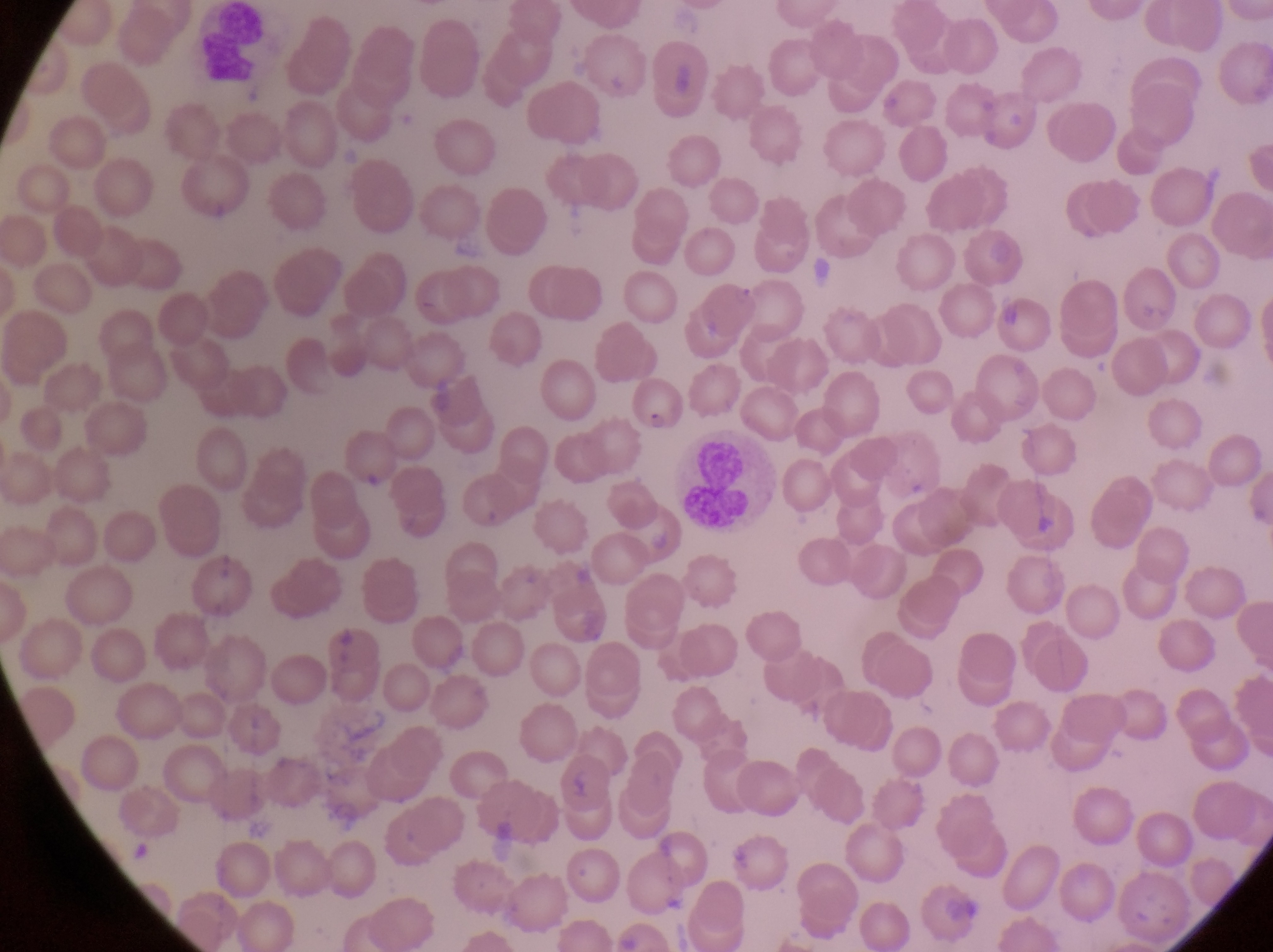 Approximate bounding boxes as (left, top, right, bottom) in pixels. Leukocyte locations: (194, 9, 274, 97), (666, 443, 773, 541). Parasitised red blood cell locations: (736, 272, 811, 340), (631, 374, 684, 436). At a magnification of 1000x. Photographed through the eyepiece of an Olympus CX-23 microscope with a smartphone camera. Collected in Uganda. Single field of view. Thin blood film. Image is 1273×952 pixels.